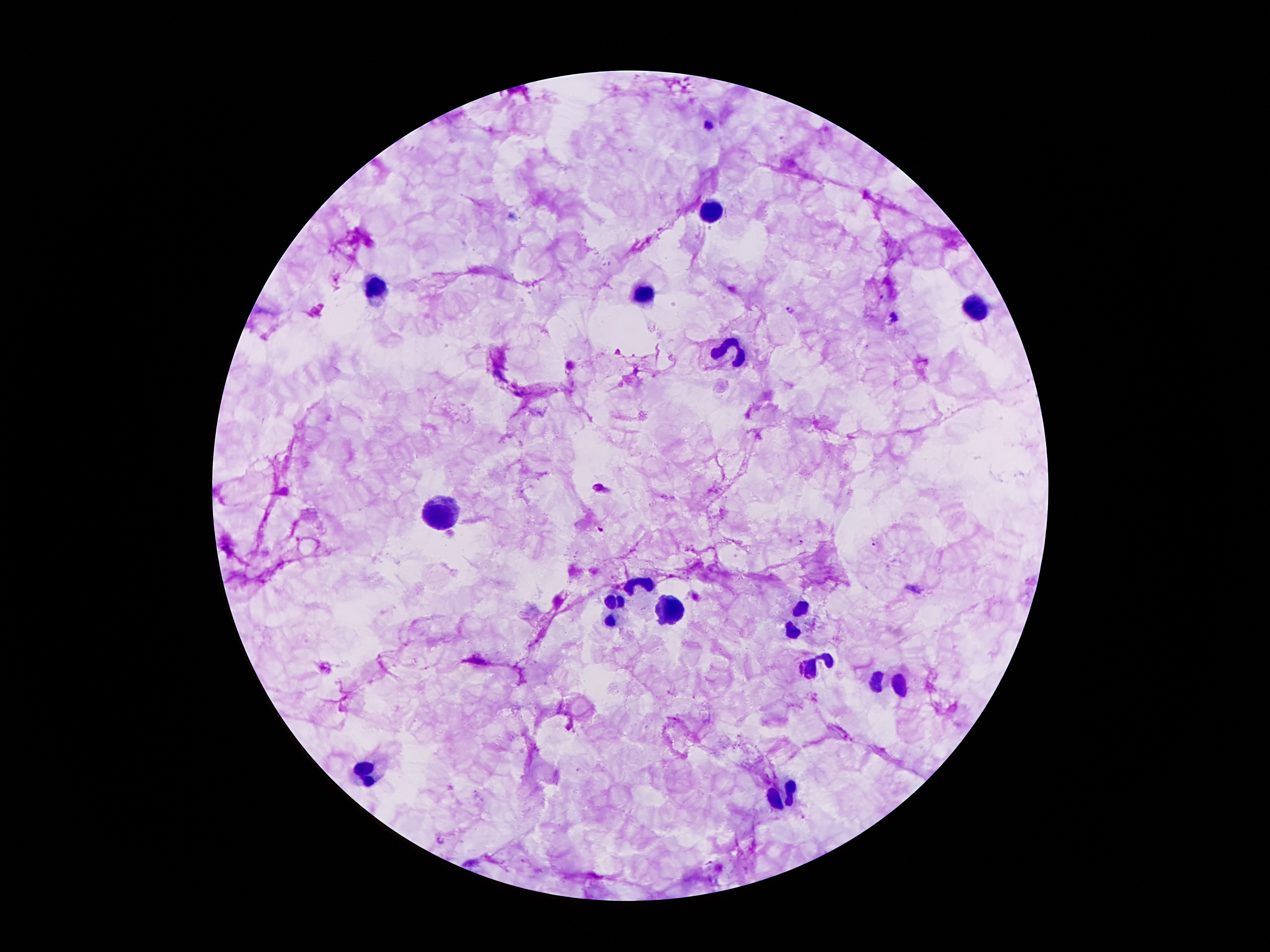 Approximate centers as {x, y} in pixels. Malaria parasite locations: {709, 124}, {790, 311}, {894, 317}, {601, 529}, {801, 542}, {873, 544}. Leukocyte locations: {710, 211}, {374, 286}, {640, 295}, {976, 313}, {738, 344}, {439, 507}, {632, 588}, {612, 605}, {674, 614}, {789, 617}, {819, 661}, {887, 686}, {366, 778}, {786, 796}. Thick peripheral-blood smear. One field from this slide. Photographed through the microscope eyepiece with a smartphone camera. Image is 1270×952 pixels. Giemsa stain. 100x magnification. Patient malaria status: positive for Plasmodium falciparum.